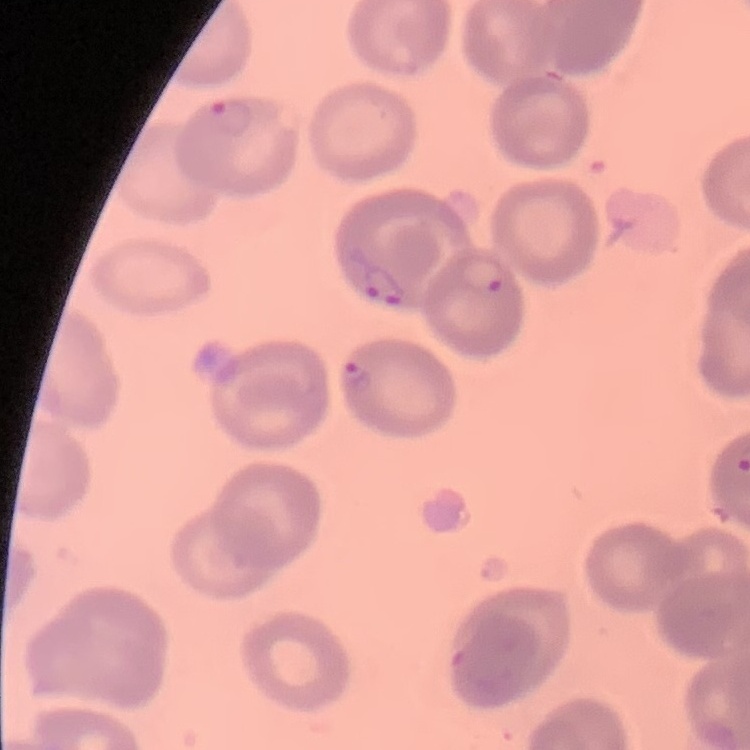

red blood cell morphology = no rouleaux formation
preparation = thin blood smear
stain = Field's or Giemsa
image type = one tile cut from a larger photomicrograph